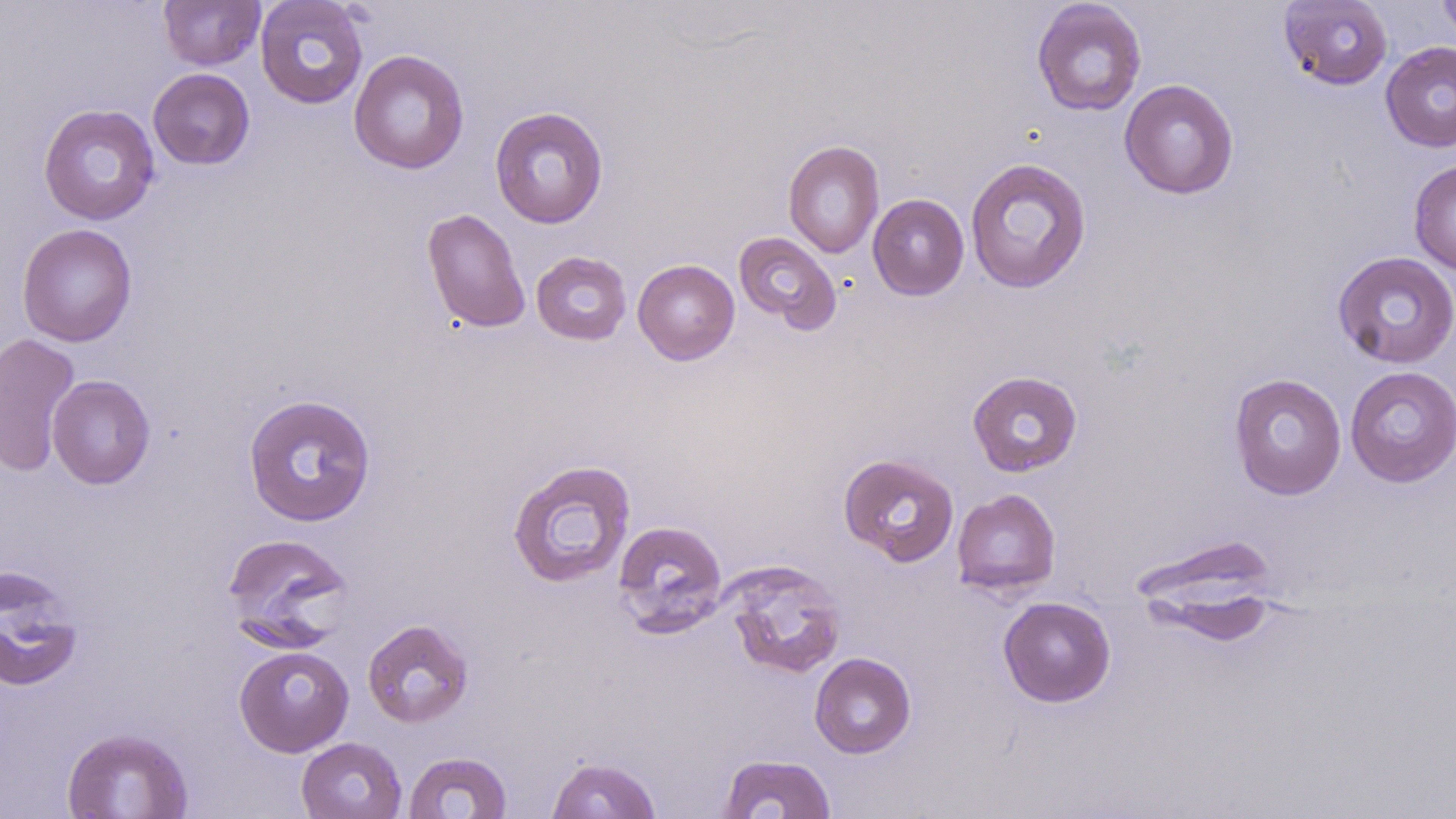 Approximate bounding boxes as (x1,y1)-(x2,y2) corner pairs in pixels. Uninfected red blood cell locations: (159,0)-(265,70), (255,0)-(368,109), (1278,0)-(1393,90), (1437,0)-(1456,48), (1031,1)-(1146,116), (1380,42)-(1456,152), (349,49)-(470,175), (148,68)-(255,170), (1118,79)-(1239,199), (38,104)-(161,225), (490,105)-(609,228), (783,139)-(884,258), (965,156)-(1092,294), (1408,158)-(1456,276), (868,194)-(969,300), (422,208)-(530,333), (17,223)-(137,347), (732,231)-(842,334), (1332,250)-(1456,369), (531,251)-(632,345), (633,259)-(740,365), (0,333)-(81,476), (1345,365)-(1456,487), (967,370)-(1083,477), (1228,372)-(1347,500), (47,374)-(156,489), (242,393)-(377,527), (838,453)-(960,567), (507,459)-(636,589), (951,488)-(1061,598), (612,520)-(728,636), (221,532)-(354,645), (1131,535)-(1281,634), (721,559)-(847,679), (0,566)-(83,692), (998,596)-(1116,707), (362,618)-(474,728), (234,644)-(354,756), (809,652)-(916,758), (61,726)-(194,818), (296,737)-(406,819), (403,751)-(512,818), (718,753)-(837,818), (546,756)-(662,818). Slide-level diagnosis: negative for blood parasites. Light microscopy. Thin blood film. Image is 1456×819 pixels. 1000x magnification. Single field of view. May-Grünwald-Giemsa stain.